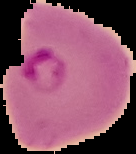

image type = cell region segmented out of the field of view; surrounding area masked to black
malaria status = parasitized
preparation = thin blood smear
image size = 136×154 pixels